State the blood parasite species.
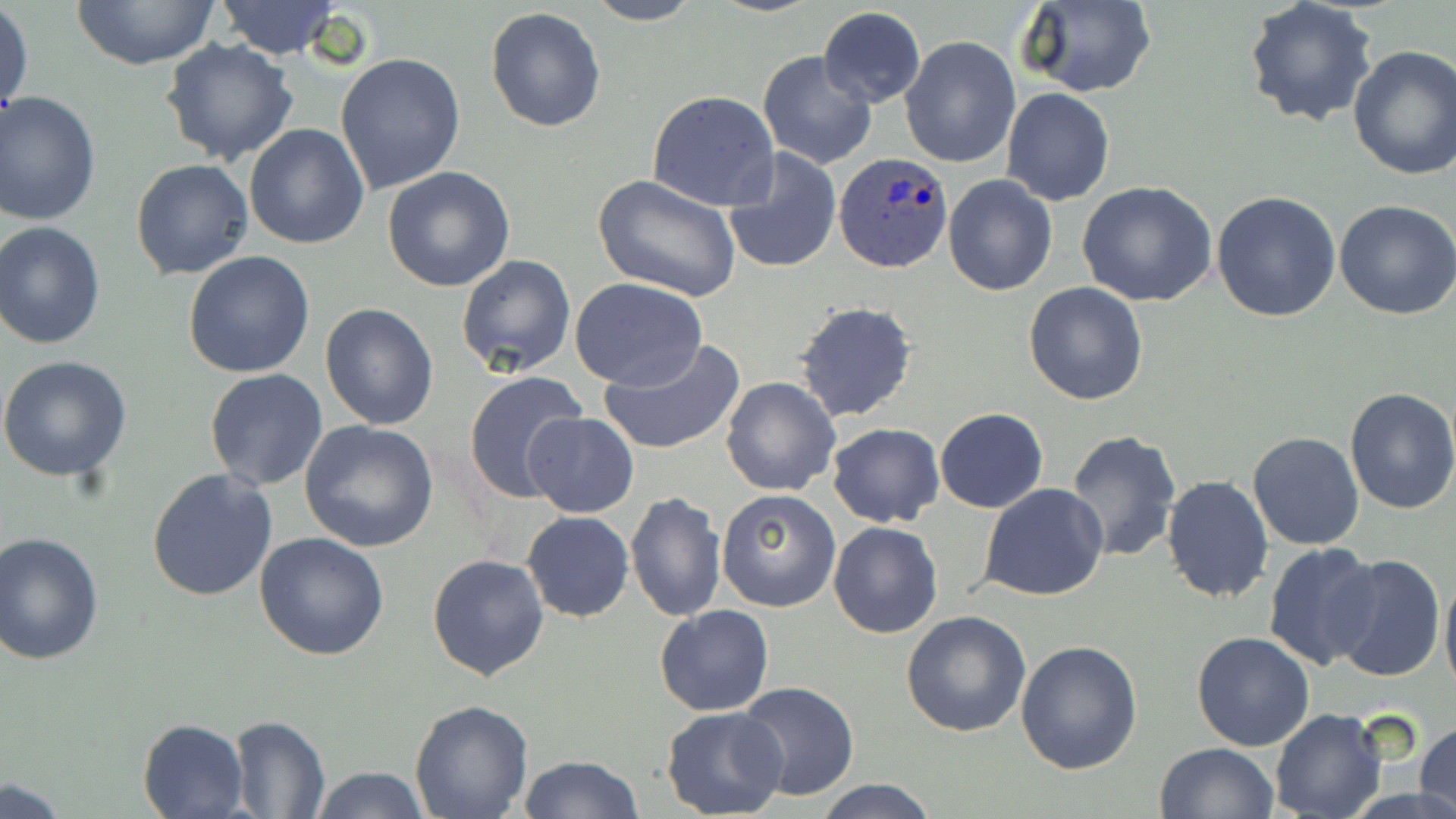
Plasmodium ovale.

Approximate bounding boxes as [x1, y1, x2, y2] in pixels. Uninfected red blood cell locations: [67, 0, 221, 69], [582, 0, 704, 25], [214, 1, 343, 59], [1016, 1, 1158, 98], [1243, 1, 1378, 129], [1, 4, 34, 125], [485, 6, 607, 133], [818, 7, 926, 108], [898, 36, 1019, 169], [160, 39, 301, 169], [1346, 46, 1456, 180], [757, 49, 877, 170], [335, 53, 466, 196], [1002, 89, 1115, 206], [646, 91, 779, 212], [0, 92, 101, 225], [243, 122, 369, 250], [722, 148, 842, 275], [130, 158, 253, 279], [382, 166, 516, 293], [593, 174, 740, 301], [942, 174, 1059, 295], [1076, 179, 1218, 306], [1211, 191, 1343, 323], [1334, 199, 1456, 319], [0, 222, 106, 351], [183, 250, 315, 377], [456, 253, 577, 377], [569, 276, 707, 389], [1023, 281, 1150, 405], [793, 300, 919, 425], [319, 302, 440, 431], [599, 339, 746, 456], [0, 354, 132, 484], [204, 369, 328, 491], [463, 371, 588, 505], [720, 377, 840, 497], [1342, 386, 1456, 516], [933, 408, 1049, 512], [523, 412, 639, 518], [299, 420, 440, 553], [827, 422, 943, 527], [1065, 429, 1181, 561], [1248, 431, 1364, 550], [146, 467, 278, 599], [1160, 474, 1275, 604], [980, 484, 1109, 602], [715, 488, 840, 611], [626, 492, 725, 622], [522, 511, 634, 623], [828, 520, 943, 638], [0, 531, 105, 666], [255, 532, 389, 661], [1263, 541, 1381, 670], [427, 553, 548, 682], [1330, 554, 1446, 685], [1439, 564, 1456, 701], [654, 604, 774, 716], [902, 609, 1032, 737], [1191, 632, 1315, 752], [1016, 639, 1144, 775], [734, 682, 860, 801], [409, 698, 534, 818], [660, 706, 788, 819], [1269, 710, 1388, 819], [227, 715, 330, 818], [137, 717, 251, 819], [1416, 720, 1456, 819], [1155, 742, 1278, 819], [517, 755, 643, 819], [309, 765, 431, 819], [814, 778, 942, 818], [0, 779, 72, 819]. Plasmodium ovale-infected red blood cell locations: [834, 152, 954, 273]. May-Grünwald-Giemsa stain. One field of a larger specimen. Captured at 1000x magnification. Image is 1456×819 pixels. Light microscopy. Thin blood film.